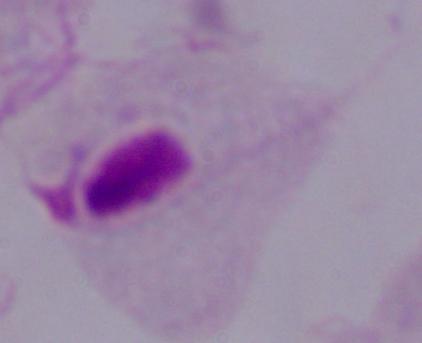

Captured at 1000x magnification. A trichomonad is shown. Photomicrograph.